Assess the morphology of the red blood cells.
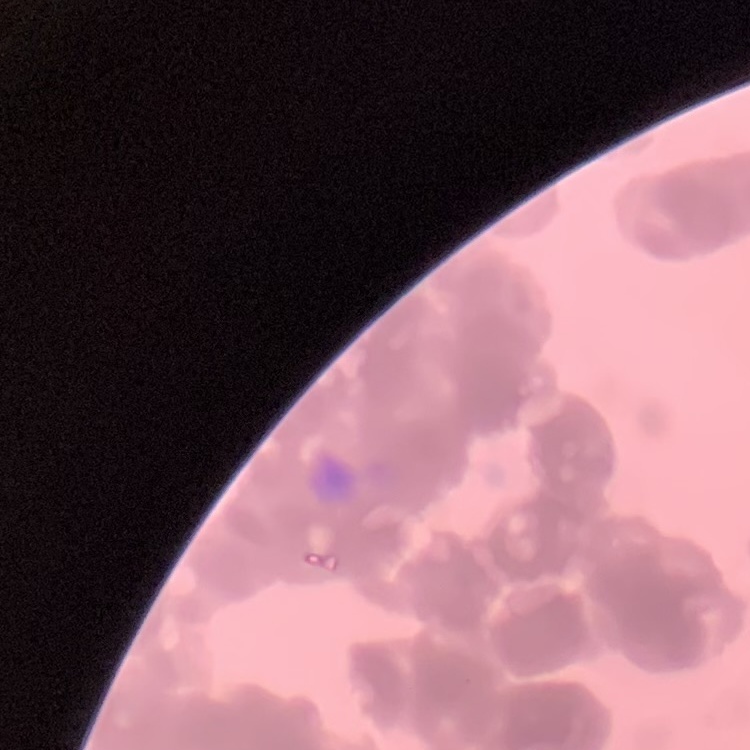

They show rouleaux formation.

Summary:
  - Preparation: thin peripheral smear
  - Stain: Field's or Giemsa
  - Image type: square crop of a larger photomicrograph